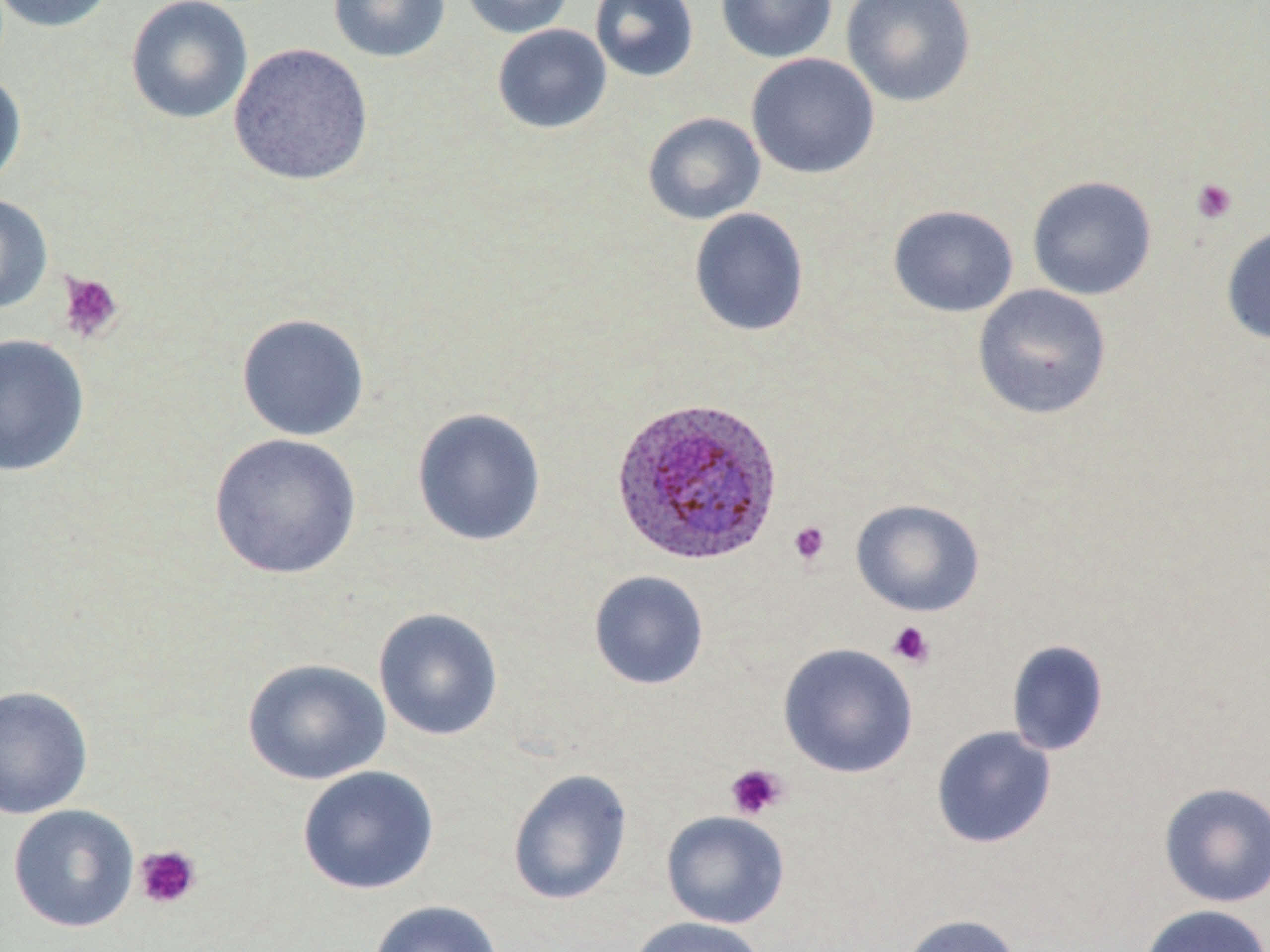

Approximate bounding boxes as (x1, y1, x2, y2) in pixels. Plasmodium ovale-infected red blood cell locations: (611, 396, 784, 566). Platelet locations: (1191, 178, 1238, 224), (57, 271, 124, 344), (788, 521, 831, 566), (887, 621, 935, 669), (725, 763, 789, 820), (133, 844, 202, 910). Uninfected red blood cell locations: (0, 0, 117, 33), (125, 0, 253, 124), (328, 0, 450, 63), (460, 0, 574, 39), (590, 0, 699, 82), (715, 0, 837, 63), (841, 0, 977, 108), (492, 24, 612, 134), (228, 42, 373, 187), (746, 53, 880, 179), (0, 70, 27, 193), (642, 112, 766, 224), (1026, 175, 1157, 301), (0, 193, 53, 314), (888, 204, 1019, 317), (689, 207, 809, 336), (1221, 225, 1270, 346), (973, 284, 1112, 420), (236, 313, 371, 442), (0, 333, 90, 476), (412, 407, 547, 547), (209, 433, 362, 579), (851, 499, 985, 617), (588, 570, 709, 690), (373, 607, 504, 741), (1006, 639, 1110, 756), (778, 643, 918, 778), (242, 658, 391, 786), (0, 685, 93, 819), (931, 726, 1057, 849), (297, 765, 440, 895), (507, 768, 633, 906), (1158, 781, 1270, 908), (8, 804, 140, 933), (661, 810, 790, 929), (368, 900, 504, 952), (1138, 903, 1269, 952), (899, 913, 1023, 952), (626, 916, 768, 952). Slide-level diagnosis: Plasmodium ovale. Light microscopy. Image is 1270×952 pixels. May-Grünwald-Giemsa-stained preparation. Single field of view. Thin blood film. Captured at 1000x magnification.